Outline each Plasmodium falciparum-infected red blood cell.
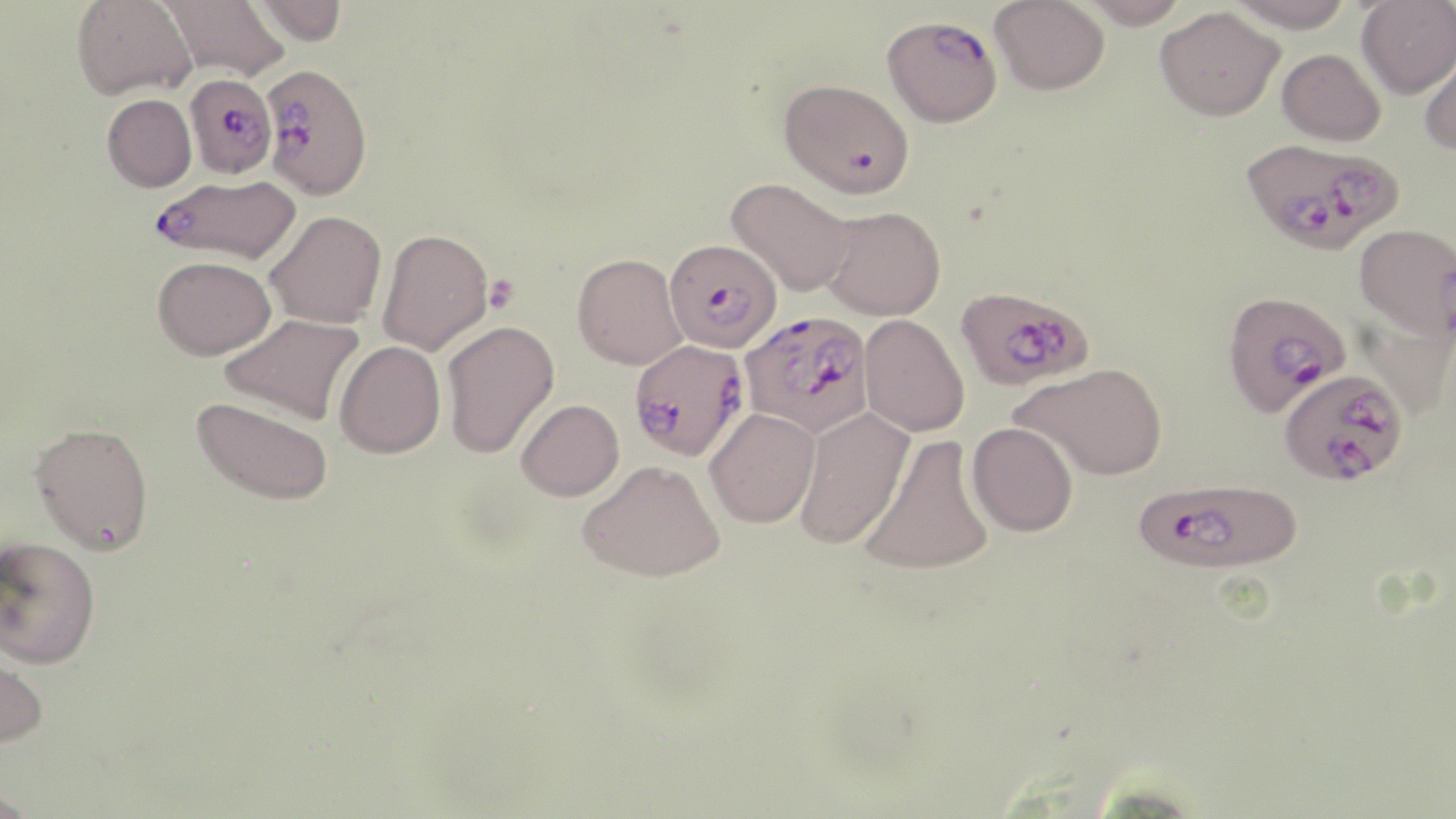

Approximate bounding boxes as [x1, y1, x2, y2] in pixels.
Plasmodium falciparum-infected red blood cells: [882, 15, 1002, 127], [260, 63, 373, 200], [184, 73, 278, 179], [779, 78, 914, 198], [1241, 136, 1405, 255], [150, 175, 301, 264], [668, 239, 779, 355], [955, 284, 1094, 391], [1228, 297, 1347, 416], [738, 310, 876, 439], [628, 338, 750, 461], [1279, 366, 1408, 484], [1133, 477, 1302, 575].

slide-level diagnosis = Plasmodium falciparum
modality = optical microscopy
uninfected red blood cell locations = approximate bounding boxes as [x1, y1, x2, y2] in pixels: [72, 0, 196, 100], [158, 0, 289, 81], [252, 0, 347, 46], [990, 0, 1110, 95], [1080, 0, 1189, 28], [1228, 0, 1355, 32], [1356, 1, 1456, 98], [1155, 6, 1284, 120], [1418, 41, 1456, 155], [1277, 48, 1386, 147], [101, 94, 197, 192], [726, 177, 855, 297], [819, 206, 946, 321], [265, 210, 387, 329], [1355, 223, 1456, 339], [377, 227, 493, 356], [572, 253, 687, 369], [152, 255, 276, 360], [220, 313, 364, 425], [859, 314, 970, 438], [441, 320, 559, 458], [334, 340, 445, 459], [1013, 362, 1168, 480], [193, 397, 334, 506], [516, 399, 624, 501], [795, 407, 914, 549], [705, 408, 821, 528], [966, 421, 1078, 536], [30, 422, 154, 554], [859, 435, 994, 576], [578, 459, 725, 582], [0, 536, 101, 669], [0, 646, 49, 750], [0, 782, 40, 819]
platelet locations = approximate bounding boxes as [x1, y1, x2, y2] in pixels: [483, 274, 520, 313]
field of view = single
stain = May-Grünwald-Giemsa
magnification = 1000x
image size = 1456×819 pixels
preparation = thin blood film